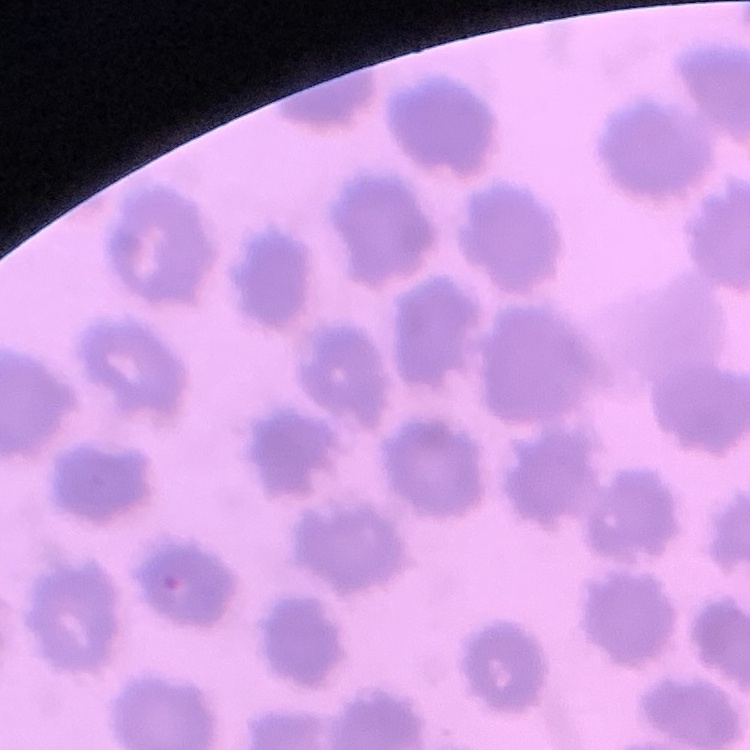
The red blood cells exhibit no rouleaux formation. Field's or Giemsa stain. Thin blood smear. One tile cut from a larger photomicrograph.